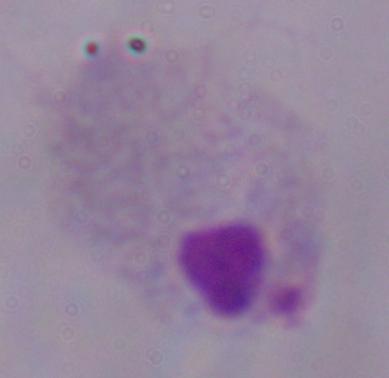

{
  "modality": "micrograph",
  "magnification": "1000x",
  "identification": "trichomonad"
}